Report the malaria status of this cell.
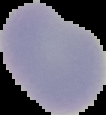

Uninfected.

preparation = thin blood smear
image size = 106×115 pixels
image type = segmented cell region on a black background